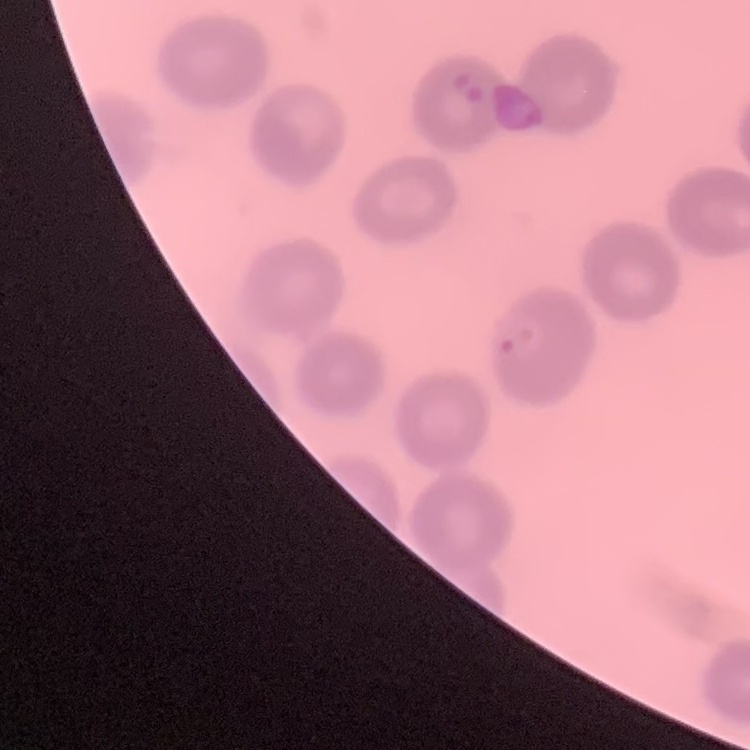

erythrocyte_morphology: no rouleaux formation
preparation: thin blood film
stain: Field's or Giemsa
image_type: one tile cut from a larger photomicrograph